Give the extent of all white blood cells.
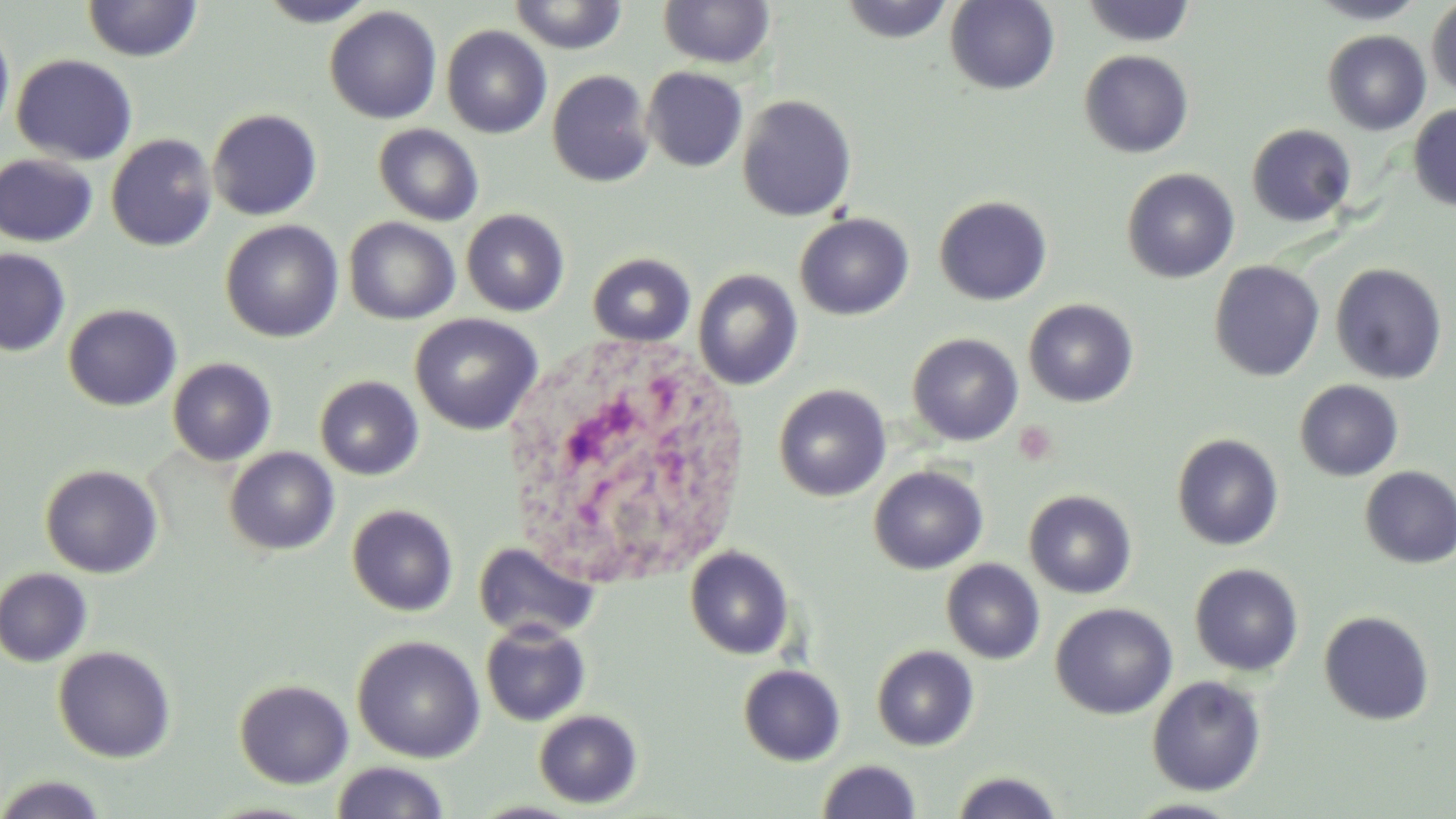
Approximate bounding boxes as (x1,y1)-(x2,y2) corner pairs in pixels.
White blood cells: (505,336)-(744,597).

Summary:
  - Uninfected red blood cell locations: (255,0)-(378,27), (508,0)-(630,54), (658,0)-(775,69), (838,0)-(955,43), (945,0)-(1060,95), (1082,0)-(1197,47), (1308,0)-(1427,24), (1426,0)-(1456,96), (82,1)-(202,62), (324,6)-(442,124), (0,19)-(15,142), (441,25)-(551,138), (1322,30)-(1431,135), (1079,50)-(1194,158), (11,54)-(137,166), (642,66)-(748,172), (546,69)-(655,188), (737,95)-(857,222), (1408,104)-(1456,211), (207,109)-(323,220), (1246,123)-(1357,227), (373,124)-(484,226), (106,133)-(218,252), (0,154)-(99,247), (1122,168)-(1240,283), (934,195)-(1053,305), (461,209)-(570,316), (794,212)-(914,320), (343,217)-(460,324), (220,220)-(343,342), (0,247)-(71,356), (587,253)-(696,347), (1208,261)-(1325,381), (1330,263)-(1447,384), (693,269)-(803,389), (1023,299)-(1139,408), (62,303)-(182,412), (409,313)-(543,435), (907,333)-(1023,446), (167,357)-(276,466), (314,375)-(424,480), (1294,379)-(1404,481), (773,384)-(891,502), (1171,433)-(1284,551), (225,446)-(339,556), (40,463)-(163,578), (868,465)-(988,574), (1360,466)-(1456,568), (1024,490)-(1137,599), (347,504)-(458,616), (473,541)-(599,643), (684,545)-(795,660), (941,559)-(1045,664), (1189,563)-(1305,676), (0,567)-(94,667), (1050,603)-(1177,719), (1318,610)-(1435,726), (480,620)-(591,726), (352,634)-(485,763), (871,644)-(979,751), (53,646)-(175,763), (738,664)-(846,766), (1147,675)-(1267,796), (234,678)-(354,788), (533,709)-(642,808), (817,759)-(921,819), (330,761)-(451,819), (949,771)-(1066,818), (0,773)-(109,819), (1122,798)-(1247,818)
  - Slide-level diagnosis: negative for blood parasites
  - Magnification: 1000x
  - Preparation: thin blood film
  - Field of view: single
  - Stain: May-Grünwald-Giemsa
  - Modality: light microscopy
  - Image size: 1456×819 pixels